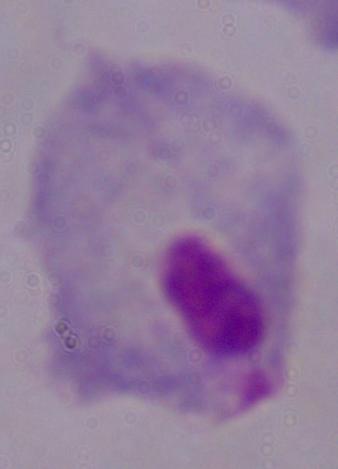
magnification: 1000x
identification: trichomonad
modality: micrograph